Report the malaria status of this cell.
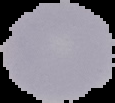

It is uninfected.

preparation = thin blood film
image type = cell region segmented out of the field of view; surrounding area masked to black
image size = 115×103 pixels